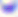
Toxoplasma gondii is shown. Captured at 400x magnification. Photomicrograph.